Point out cells.
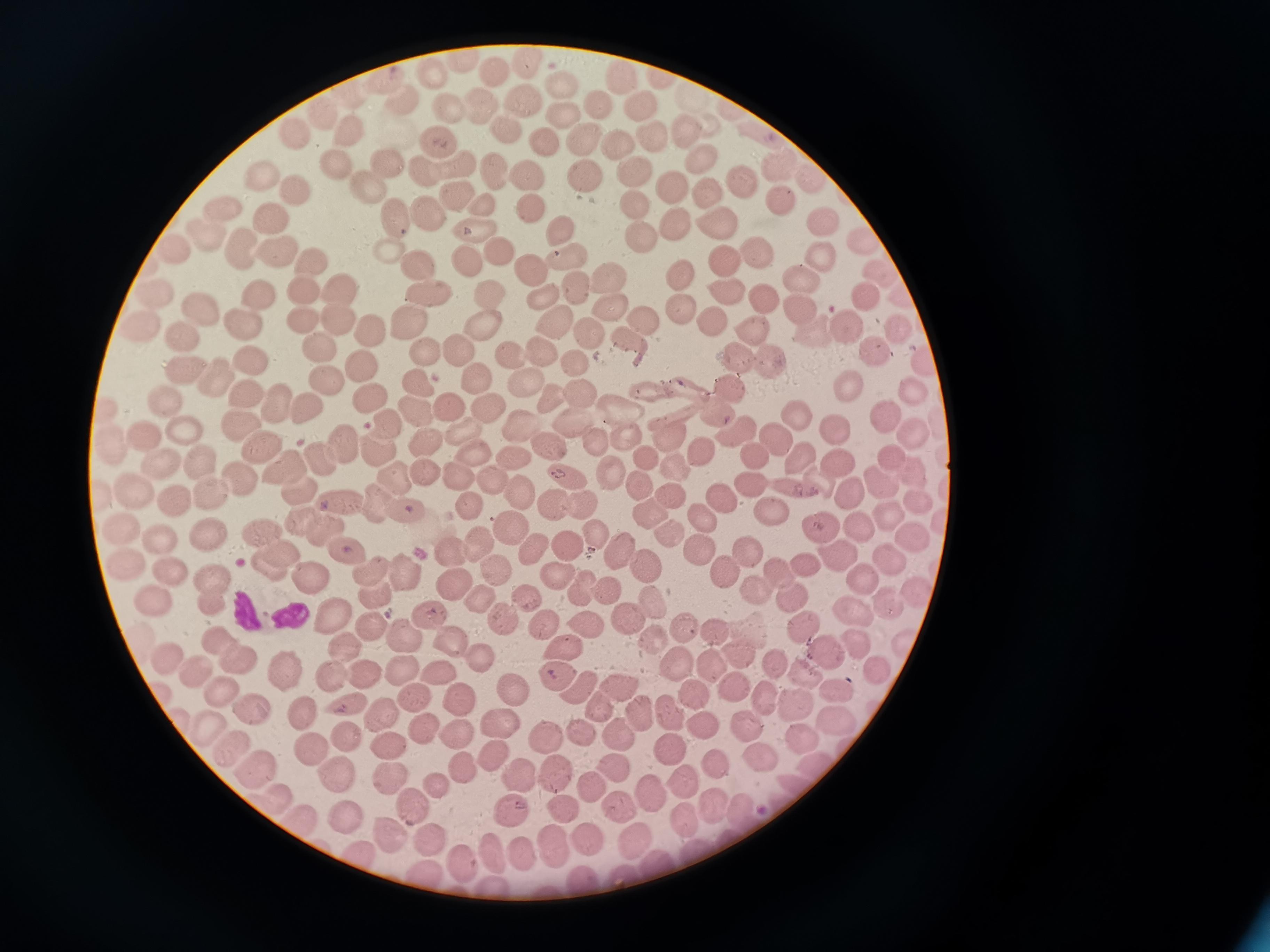
Approximate object centers, in pixels from the top-left corner.
Cells: (x=461, y=60), (x=491, y=72), (x=428, y=73), (x=620, y=77), (x=663, y=80), (x=376, y=82), (x=562, y=88), (x=396, y=99), (x=479, y=102), (x=688, y=102), (x=599, y=104), (x=634, y=104), (x=522, y=106), (x=445, y=108), (x=320, y=113), (x=562, y=115), (x=686, y=129), (x=343, y=131), (x=505, y=131), (x=652, y=132), (x=295, y=134), (x=759, y=136), (x=581, y=137), (x=542, y=138), (x=434, y=141), (x=618, y=145), (x=698, y=157), (x=384, y=165), (x=452, y=165), (x=327, y=166), (x=777, y=168), (x=422, y=170), (x=584, y=172), (x=499, y=174), (x=630, y=174), (x=809, y=175), (x=528, y=176), (x=266, y=180), (x=361, y=181), (x=737, y=181), (x=669, y=182), (x=708, y=193), (x=450, y=194), (x=292, y=195), (x=634, y=198), (x=778, y=199), (x=223, y=205), (x=481, y=206), (x=425, y=207), (x=529, y=208), (x=396, y=216), (x=265, y=221), (x=821, y=222), (x=672, y=225), (x=716, y=226), (x=476, y=229), (x=558, y=230), (x=210, y=235), (x=641, y=236), (x=860, y=243), (x=382, y=247), (x=177, y=249), (x=242, y=250), (x=497, y=250), (x=753, y=251), (x=273, y=254), (x=819, y=255), (x=566, y=258), (x=721, y=258), (x=411, y=259), (x=310, y=260), (x=464, y=260), (x=681, y=270), (x=527, y=271), (x=608, y=274), (x=873, y=274), (x=798, y=279), (x=298, y=288), (x=572, y=288), (x=343, y=289), (x=724, y=289), (x=426, y=290), (x=253, y=294), (x=862, y=294), (x=150, y=295), (x=488, y=297), (x=761, y=298), (x=542, y=303), (x=609, y=305), (x=197, y=308), (x=675, y=310), (x=798, y=310), (x=405, y=317), (x=296, y=319), (x=335, y=319), (x=239, y=321), (x=637, y=321), (x=709, y=321), (x=844, y=324), (x=550, y=325), (x=136, y=326), (x=748, y=328), (x=896, y=329), (x=478, y=330), (x=587, y=331), (x=177, y=332), (x=816, y=332), (x=366, y=333), (x=624, y=340), (x=313, y=342), (x=868, y=349), (x=455, y=351), (x=536, y=351), (x=426, y=352), (x=733, y=354), (x=923, y=358), (x=358, y=360), (x=509, y=361), (x=251, y=362), (x=572, y=362), (x=769, y=366), (x=181, y=368), (x=215, y=376), (x=327, y=379), (x=473, y=381), (x=847, y=383), (x=681, y=384), (x=417, y=386), (x=521, y=387), (x=730, y=387), (x=649, y=388), (x=241, y=389), (x=910, y=389), (x=576, y=396), (x=161, y=398), (x=550, y=399), (x=368, y=401), (x=272, y=403), (x=482, y=406), (x=305, y=408), (x=449, y=409), (x=624, y=409), (x=884, y=410), (x=103, y=411), (x=715, y=412), (x=419, y=415), (x=789, y=417), (x=382, y=422), (x=237, y=423), (x=828, y=424), (x=570, y=426), (x=521, y=427), (x=178, y=428), (x=744, y=428), (x=729, y=429), (x=912, y=431), (x=141, y=433), (x=664, y=433), (x=458, y=436), (x=625, y=437), (x=772, y=439), (x=420, y=441), (x=598, y=441), (x=338, y=442), (x=373, y=444), (x=698, y=445), (x=259, y=446), (x=550, y=447), (x=108, y=450), (x=747, y=453), (x=317, y=454), (x=641, y=455), (x=514, y=457), (x=837, y=457), (x=479, y=458), (x=889, y=458), (x=798, y=460), (x=198, y=461), (x=672, y=465), (x=156, y=466), (x=606, y=466), (x=280, y=470), (x=912, y=470), (x=421, y=472), (x=453, y=475), (x=389, y=476), (x=565, y=476), (x=878, y=480), (x=234, y=481), (x=820, y=482), (x=489, y=483), (x=635, y=483), (x=752, y=483), (x=297, y=487), (x=133, y=490), (x=208, y=490), (x=517, y=490), (x=795, y=491), (x=851, y=495), (x=674, y=496), (x=720, y=498), (x=919, y=498), (x=338, y=501), (x=372, y=501), (x=172, y=502), (x=464, y=505), (x=550, y=505), (x=576, y=506), (x=401, y=508), (x=769, y=509), (x=648, y=512), (x=890, y=514), (x=704, y=517), (x=302, y=520), (x=860, y=526), (x=121, y=527), (x=820, y=527), (x=321, y=529), (x=507, y=529), (x=662, y=530), (x=263, y=531), (x=591, y=533), (x=207, y=535), (x=913, y=535), (x=158, y=541), (x=470, y=544), (x=567, y=545), (x=699, y=545), (x=745, y=546), (x=344, y=548), (x=527, y=549), (x=444, y=550), (x=277, y=553), (x=615, y=553), (x=835, y=557), (x=804, y=559), (x=888, y=559), (x=124, y=564), (x=261, y=565), (x=649, y=566), (x=166, y=567), (x=489, y=569), (x=369, y=570), (x=406, y=570), (x=552, y=573), (x=782, y=574), (x=863, y=574), (x=304, y=577), (x=726, y=577), (x=210, y=579), (x=453, y=584), (x=580, y=588), (x=604, y=590), (x=756, y=591), (x=915, y=591), (x=378, y=593), (x=522, y=594), (x=791, y=597), (x=650, y=598), (x=478, y=599), (x=211, y=601), (x=886, y=601), (x=151, y=602), (x=853, y=612), (x=432, y=617), (x=334, y=619), (x=626, y=621), (x=502, y=623), (x=540, y=624), (x=686, y=625), (x=583, y=627), (x=802, y=628), (x=374, y=629), (x=712, y=632), (x=403, y=635), (x=653, y=637), (x=215, y=638), (x=141, y=640), (x=907, y=640), (x=858, y=642), (x=454, y=647), (x=824, y=650), (x=564, y=652), (x=345, y=653), (x=736, y=656), (x=166, y=657), (x=676, y=657), (x=237, y=659), (x=482, y=659), (x=711, y=664), (x=284, y=666), (x=773, y=666), (x=191, y=669), (x=404, y=669), (x=878, y=670), (x=803, y=671), (x=327, y=674), (x=441, y=674), (x=360, y=675), (x=557, y=678), (x=575, y=686), (x=736, y=687), (x=837, y=687), (x=619, y=688), (x=515, y=690), (x=693, y=693), (x=223, y=694), (x=765, y=698), (x=414, y=699), (x=460, y=700), (x=797, y=700), (x=341, y=705), (x=251, y=706), (x=597, y=706), (x=670, y=711), (x=298, y=712), (x=637, y=712), (x=379, y=716), (x=501, y=716), (x=839, y=716), (x=743, y=725), (x=708, y=726), (x=619, y=727), (x=204, y=728), (x=339, y=730), (x=419, y=731), (x=581, y=732), (x=455, y=733), (x=799, y=737), (x=537, y=738), (x=668, y=743), (x=389, y=744), (x=230, y=745), (x=309, y=746), (x=494, y=751), (x=757, y=751), (x=814, y=761), (x=716, y=763), (x=617, y=765), (x=464, y=766), (x=253, y=771), (x=333, y=772), (x=551, y=773), (x=520, y=774), (x=683, y=778), (x=392, y=779), (x=438, y=786), (x=591, y=786), (x=650, y=797), (x=279, y=801), (x=710, y=804), (x=416, y=806), (x=743, y=807), (x=508, y=808), (x=560, y=808), (x=615, y=809), (x=343, y=813), (x=679, y=815), (x=295, y=823), (x=583, y=836), (x=391, y=837), (x=431, y=838), (x=553, y=838), (x=634, y=838), (x=695, y=846), (x=485, y=849), (x=517, y=849), (x=360, y=851), (x=457, y=851), (x=651, y=861), (x=420, y=867), (x=623, y=873), (x=585, y=879), (x=492, y=891).

Summary:
  - Malaria reading: positive
  - Field of view: single
  - Stain: Giemsa
  - Preparation: thin smear
  - Capture: smartphone through the microscope eyepiece
  - Image size: 1270×952 pixels